Evaluate for malaria.
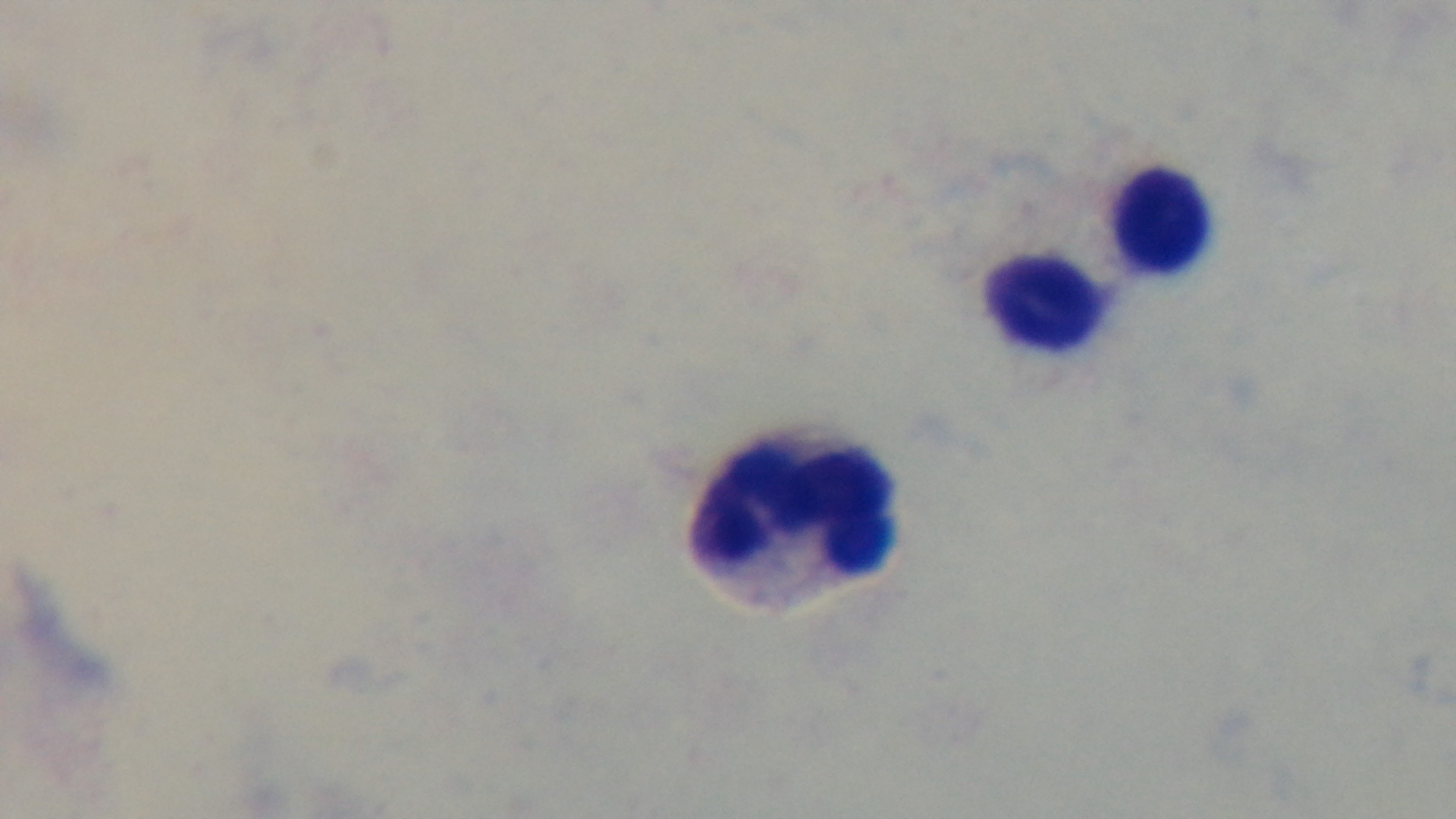
Uninfected.

Preparation: thick smear. Mounted 4K digital camera. Giemsa stain. Oil-immersion objective, 100x. Single field of view. Light microscopy.